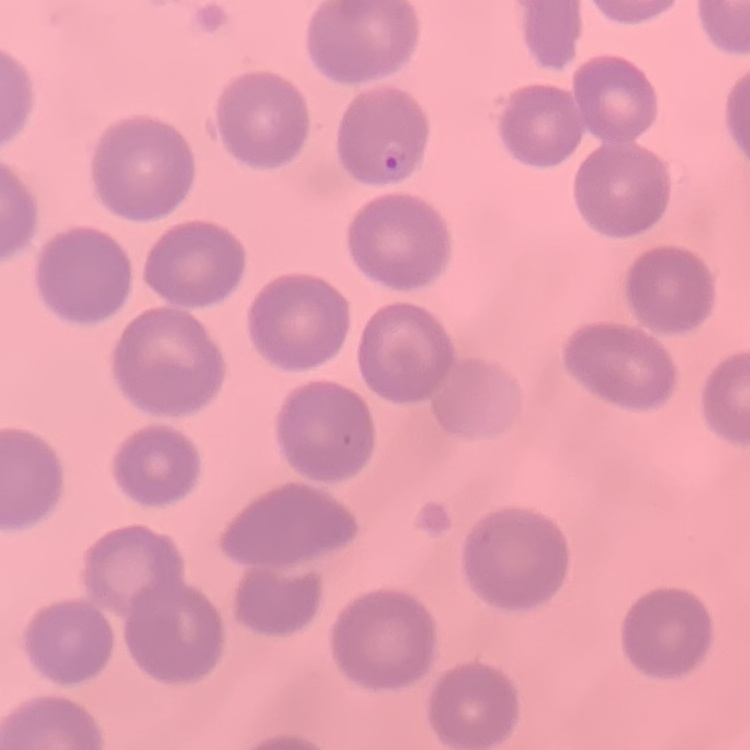
Summary:
  - Erythrocyte morphology: no rouleaux formation
  - Image type: square crop of a larger photomicrograph
  - Stain: Field's or Giemsa
  - Preparation: thin peripheral smear